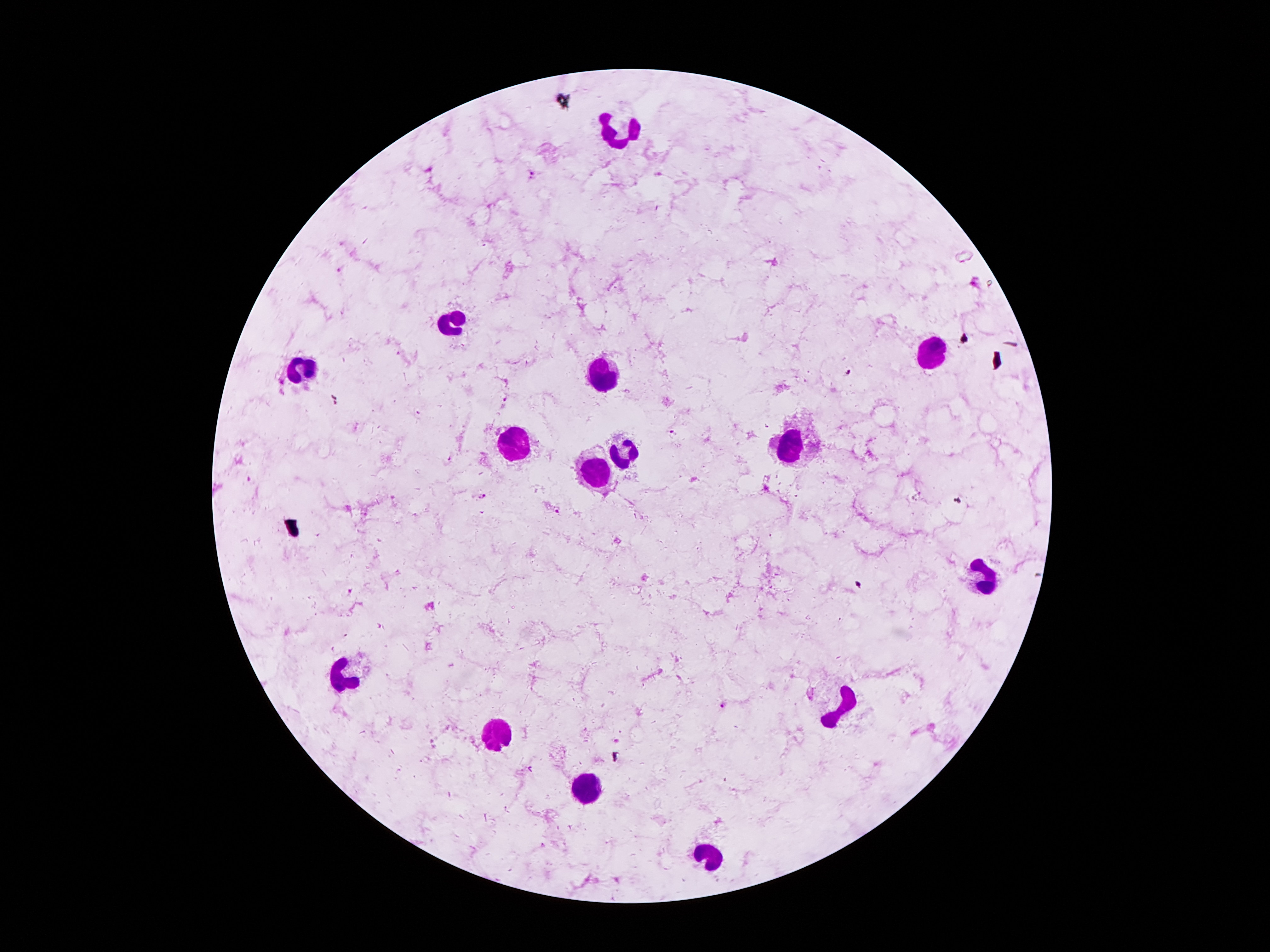

coordinate format = approximate centers as [x, y] in pixels
leukocyte locations = [624, 132], [454, 321], [932, 352], [300, 370], [607, 373], [794, 443], [512, 445], [624, 448], [596, 473], [985, 569], [351, 677], [845, 700], [493, 730], [584, 789], [706, 851]
malaria parasite locations = [530, 174], [341, 269], [976, 284], [849, 371], [672, 433], [248, 479], [486, 498], [958, 501], [556, 511], [857, 585], [351, 592], [722, 706]
magnification = 100x
preparation = thick blood smear
image size = 1270×952 pixels
capture = smartphone camera through the microscope eyepiece
field of view = one from this slide
patient malaria status = infected with Plasmodium falciparum
stain = Giemsa